Classify this cell by malaria status.
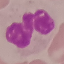

It is uninfected.

Thin blood film. Automatically extracted cell patch, resized to 64 × 64 pixels. Photographed with a smartphone camera at the microscope eyepiece. Giemsa-stained preparation.